Report the malaria status of this cell.
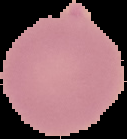

It is uninfected.

image type = segmented cell region with the area outside set to black
preparation = thin blood smear
image size = 127×139 pixels